Assess for Plasmodium parasites.
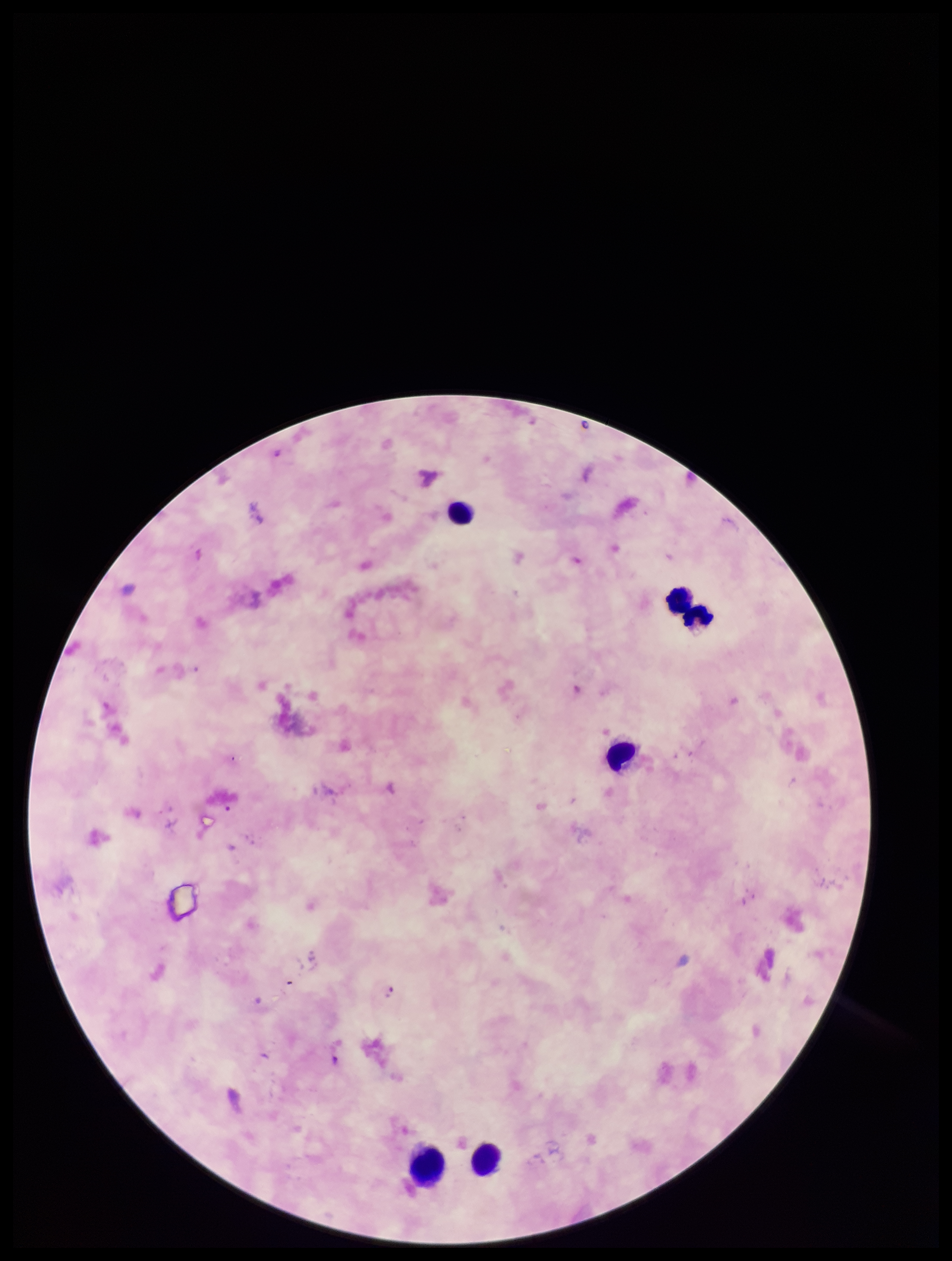
Identified.

Summary:
  - Preparation: thick smear
  - Patient malaria status: positive
  - Stain: Giemsa
  - Image size: 952×1261 pixels
  - Capture: smartphone photograph through the microscope eyepiece
  - Leukocyte count: 6
  - Parasite count: 1
  - Species reported for this patient: Plasmodium falciparum
  - Field of view: one from this slide